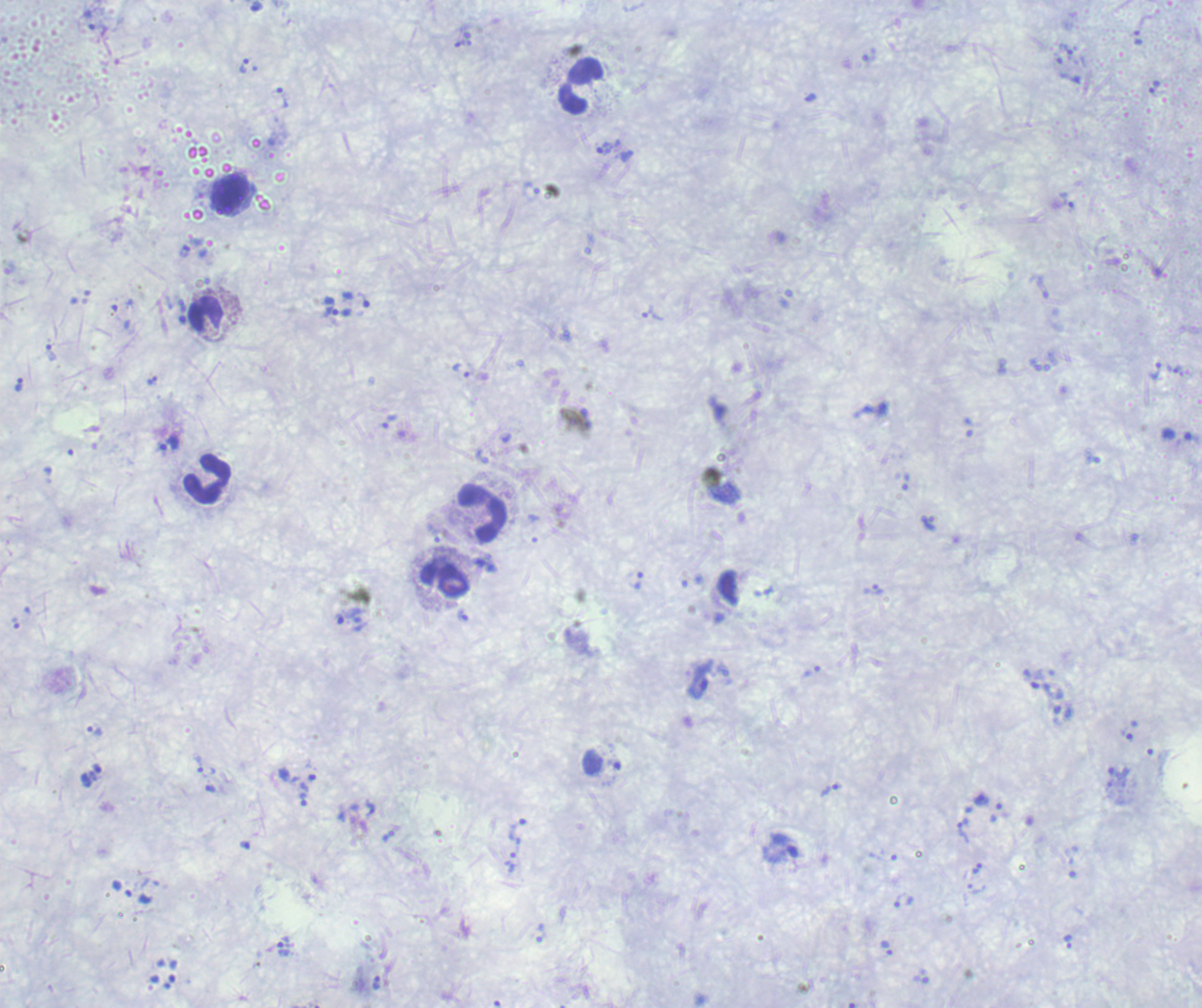
Approximate centers as {x, y} in pixels.
Summary:
  - Trophozoite locations: {1065, 49}, {244, 66}, {1154, 87}, {282, 97}, {605, 148}, {332, 311}, {652, 313}, {50, 352}, {461, 370}, {1155, 371}, {151, 380}, {19, 384}, {390, 422}, {170, 443}, {638, 580}, {873, 589}, {463, 615}, {349, 617}, {94, 731}, {199, 764}, {210, 788}, {830, 790}, {305, 794}, {981, 800}, {963, 830}, {517, 831}, {511, 862}, {976, 868}, {1068, 941}, {886, 948}, {283, 949}, {376, 982}
  - Leukocyte locations: {581, 87}, {232, 195}, {205, 315}, {208, 479}, {482, 512}, {445, 579}
  - Field of view: one from this slide
  - Context: previously used in an actual diagnosis
  - Result: malaria parasites identified
  - Magnification: 100x
  - Background quality: unsatisfactory
  - Image size: 1202×1008 pixels
  - Stain: Romanowsky
  - Preparation: thick blood smear